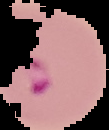

Summary:
  - Result: Plasmodium parasites detected
  - Preparation: thin blood film
  - Image size: 109×130 pixels
  - Image type: segmented cell region with the area outside set to black